Assess the morphology of the erythrocytes.
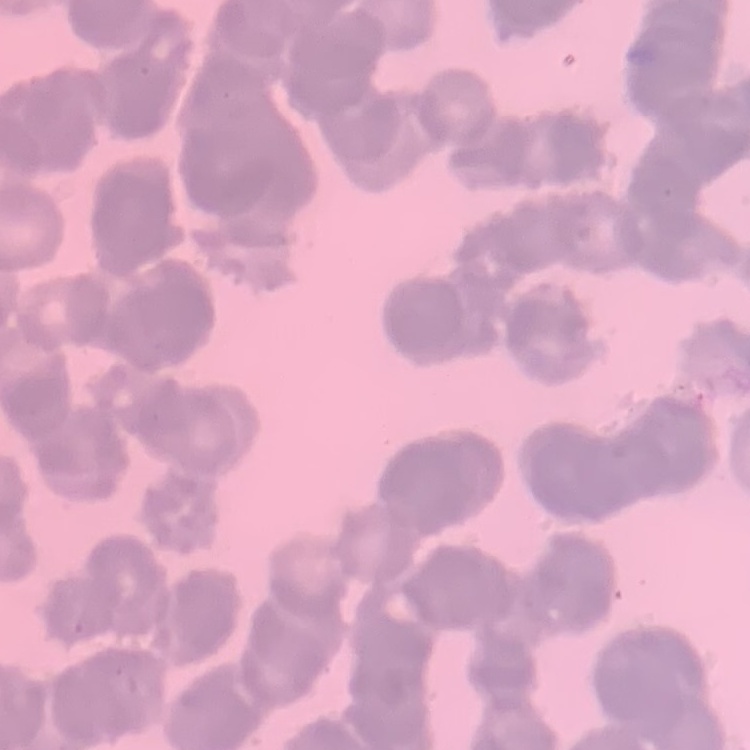
Rouleaux formation.

Thin peripheral smear. Square crop of a larger photomicrograph. Stained with either Field's or Giemsa.